Give the location of every parasitized red blood cell.
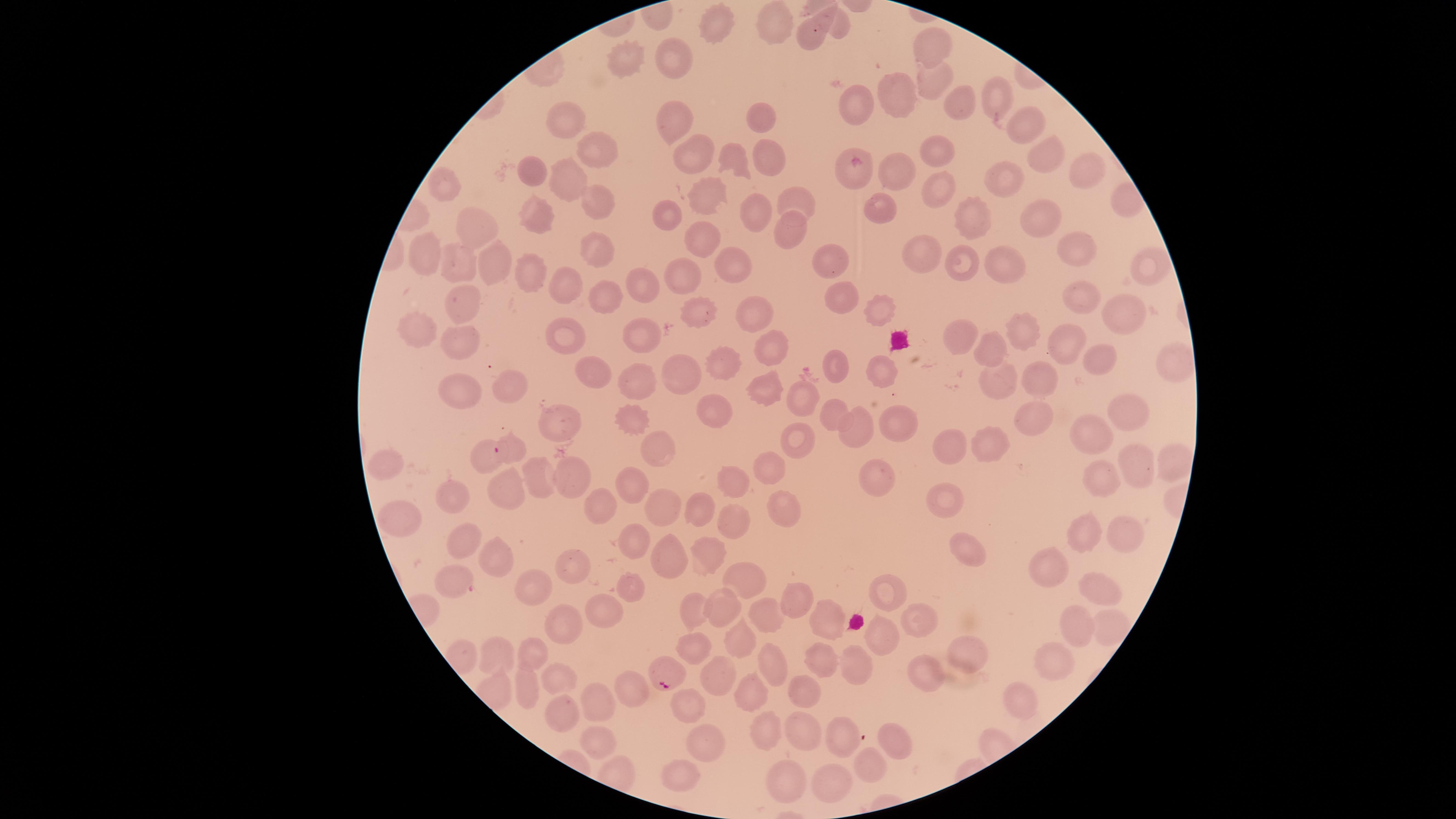

Approximate marker points as [x, y] in pixels.
Parasitized red blood cells: [855, 169], [509, 449], [454, 582], [661, 676].

Approximate marker points as [x, y] in pixels. Uninfected red blood cells: [773, 21], [707, 29], [806, 34], [930, 47], [633, 55], [676, 56], [928, 81], [894, 92], [996, 95], [958, 102], [857, 107], [670, 117], [1026, 121], [758, 122], [569, 124], [688, 149], [1041, 150], [594, 151], [763, 154], [938, 154], [729, 160], [893, 171], [1083, 171], [530, 172], [1008, 180], [565, 181], [441, 184], [932, 186], [590, 196], [706, 197], [795, 197], [879, 207], [757, 209], [975, 210], [670, 211], [538, 214], [1041, 217], [474, 227], [785, 228], [696, 241], [1069, 244], [920, 251], [429, 252], [586, 253], [461, 255], [832, 260], [1149, 264], [492, 265], [1006, 265], [734, 266], [965, 267], [685, 269], [528, 275], [643, 279], [560, 286], [602, 286], [839, 292], [1072, 297], [462, 302], [695, 310], [752, 311], [1120, 311], [882, 313], [417, 326], [1017, 330], [643, 334], [567, 335], [957, 337], [1063, 340], [462, 345], [770, 347], [985, 352], [1169, 359], [1092, 362], [714, 363], [835, 363], [875, 366], [679, 370], [597, 373], [638, 376], [997, 376], [1035, 377], [509, 380], [767, 380], [457, 389], [798, 398], [715, 408], [1127, 411], [631, 414], [839, 414], [1039, 417], [896, 424], [564, 427], [856, 429], [1095, 429], [803, 436], [947, 445], [983, 448], [656, 449], [484, 451], [1173, 461], [388, 471], [1135, 471], [765, 472], [566, 475], [1100, 475], [533, 478], [875, 480], [736, 481], [503, 482], [626, 488], [458, 498], [940, 499], [660, 503], [600, 504], [781, 504], [700, 512], [402, 519], [733, 526], [1123, 529], [1089, 531], [463, 537], [634, 539], [710, 549], [964, 549], [666, 553], [495, 555], [574, 561], [1054, 564], [740, 577], [538, 583], [631, 583], [886, 586], [1097, 586], [795, 595], [725, 602], [695, 606], [604, 607], [766, 615], [827, 620], [917, 620], [565, 621], [1118, 621], [1076, 625], [883, 631], [742, 637], [965, 642], [701, 647], [532, 650], [1054, 652], [498, 653], [778, 662], [822, 662], [854, 663], [719, 672], [562, 674], [926, 678], [529, 684], [630, 684], [753, 686], [1024, 694], [598, 695], [802, 697], [689, 704], [564, 713], [770, 722], [802, 725], [843, 733], [903, 737], [601, 741], [706, 742], [871, 761], [834, 777], [682, 779], [787, 779]. Single field of view. The visible region is circular. Species: Plasmodium falciparum. Image is 1456×819 pixels. Giemsa stain. Thin blood smear. Photographed with a smartphone camera through the microscope eyepiece.